Report the malaria status of this cell.
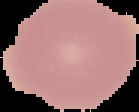
It is uninfected.

{
  "preparation": "thin blood film",
  "image_type": "segmented cell region with the area outside set to black",
  "image_size": "139×112 pixels"
}